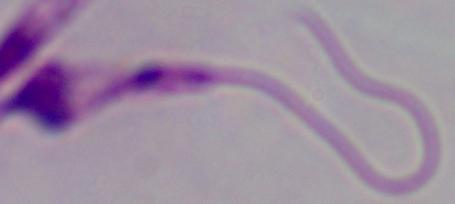

A Leishmania parasite is shown. Captured at 1000x magnification. Micrograph.